Describe the morphology of the erythrocytes.
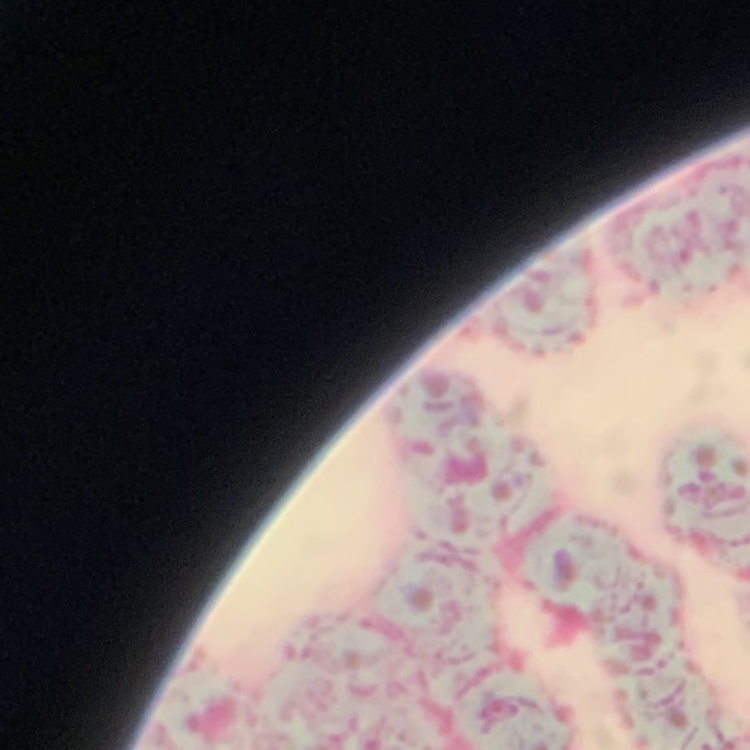
They show rouleaux formation.

Summary:
  - Stain: Field's or Giemsa
  - Image type: one tile cut from a larger photomicrograph
  - Preparation: thin peripheral smear